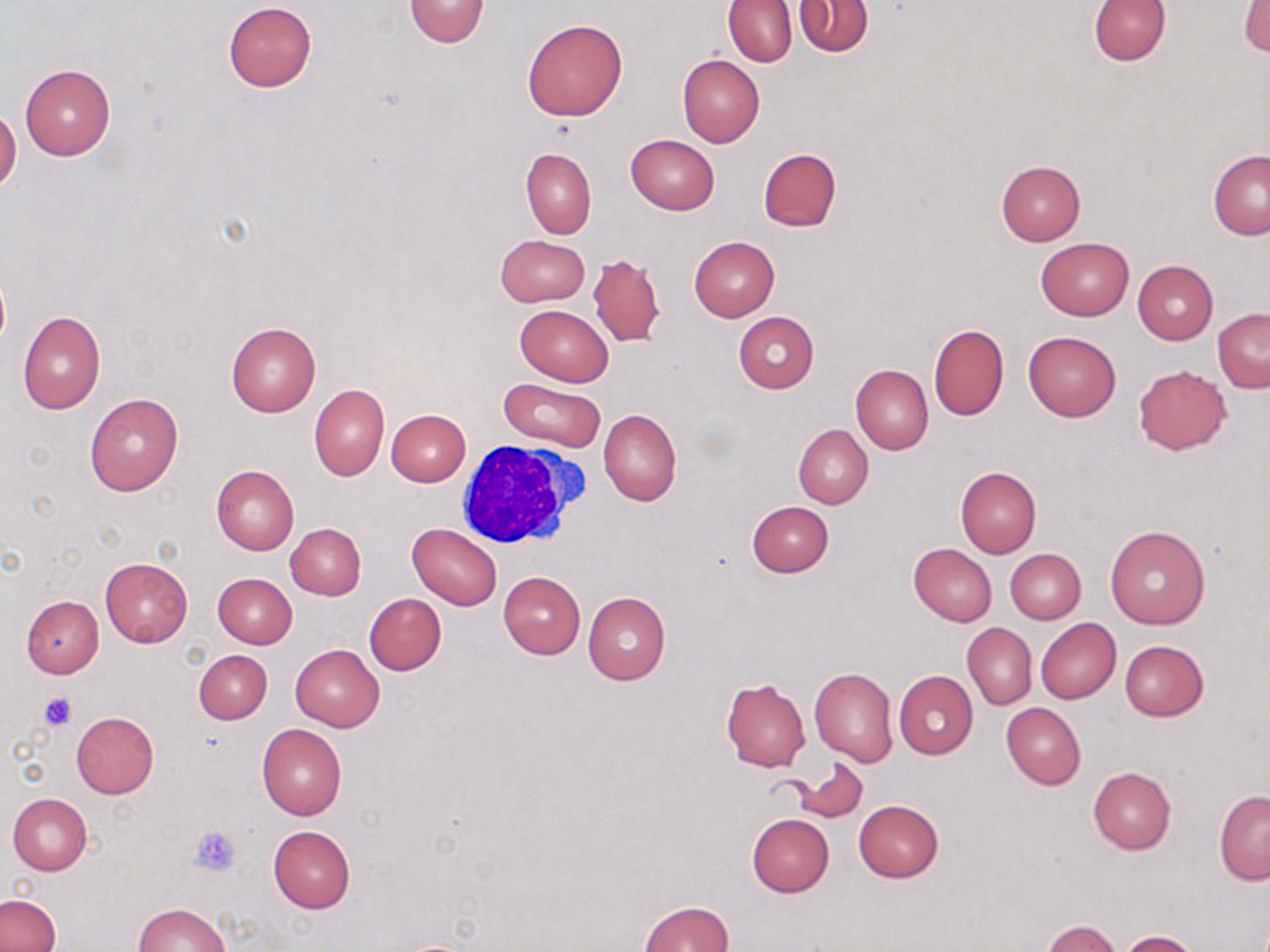

Summary:
  - Coordinate format: approximate bounding boxes as (x1, y1, x2, y2) in pixels
  - Uninfected red blood cell locations: (404, 0, 491, 47), (1087, 0, 1170, 66), (724, 1, 797, 66), (795, 1, 872, 56), (1241, 1, 1270, 55), (224, 2, 317, 92), (521, 18, 628, 121), (677, 53, 764, 147), (20, 64, 114, 160), (625, 135, 718, 215), (520, 148, 596, 238), (758, 148, 841, 232), (1209, 150, 1270, 240), (996, 159, 1086, 245), (504, 232, 594, 385), (496, 234, 588, 307), (689, 237, 779, 321), (1035, 237, 1135, 320), (588, 252, 664, 347), (1132, 260, 1217, 344), (515, 304, 614, 386), (1213, 308, 1269, 392), (17, 310, 106, 413), (733, 312, 819, 392), (226, 323, 320, 417), (928, 324, 1009, 421), (1023, 331, 1121, 421), (851, 364, 933, 454), (1133, 365, 1231, 454), (499, 378, 606, 450), (309, 383, 389, 480), (85, 394, 183, 497), (386, 408, 471, 486), (599, 408, 681, 506), (793, 424, 873, 508), (211, 464, 298, 556), (955, 466, 1040, 558), (748, 501, 833, 576), (286, 522, 366, 599), (407, 523, 503, 610), (1105, 524, 1211, 629), (909, 543, 996, 625), (1006, 549, 1085, 624), (101, 558, 192, 647), (498, 571, 585, 658), (213, 573, 297, 648), (493, 578, 663, 668), (583, 592, 670, 686), (364, 593, 446, 676), (20, 596, 104, 678), (1035, 618, 1121, 704), (963, 624, 1035, 708), (1119, 640, 1209, 721), (290, 645, 384, 731), (194, 649, 272, 724), (810, 667, 897, 767), (894, 670, 977, 758), (721, 679, 811, 772), (1001, 703, 1085, 790), (71, 712, 159, 799), (257, 724, 348, 820), (790, 758, 869, 823), (1088, 766, 1175, 854), (1213, 790, 1270, 883), (8, 793, 92, 875), (853, 800, 944, 883), (747, 813, 834, 896), (268, 826, 356, 913), (1, 894, 59, 952), (638, 901, 733, 952), (135, 902, 230, 951), (1042, 920, 1123, 951), (1121, 930, 1203, 952)
  - Platelet locations: (39, 691, 79, 732), (190, 825, 243, 876)
  - White blood cell locations: (451, 439, 587, 551)
  - Slide-level diagnosis: negative for blood parasites
  - Modality: light microscopy
  - Stain: May-Grünwald-Giemsa
  - Magnification: 1000x
  - Field of view: one of a larger specimen
  - Image size: 1270×952 pixels
  - Preparation: thin blood film